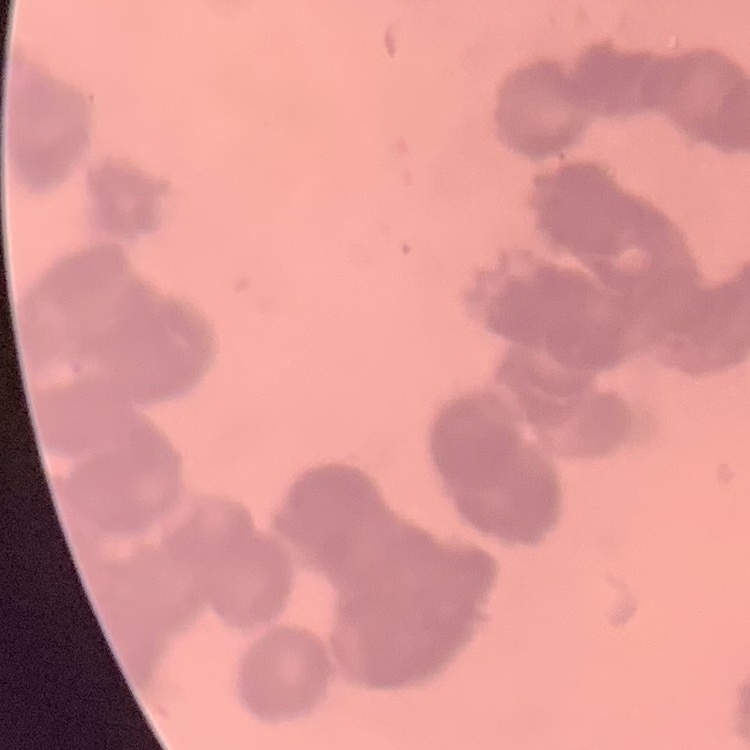

Summary:
  - Red blood cell morphology: rouleaux formation
  - Preparation: thin peripheral smear
  - Stain: Field's or Giemsa
  - Image type: one tile cut from a larger photomicrograph